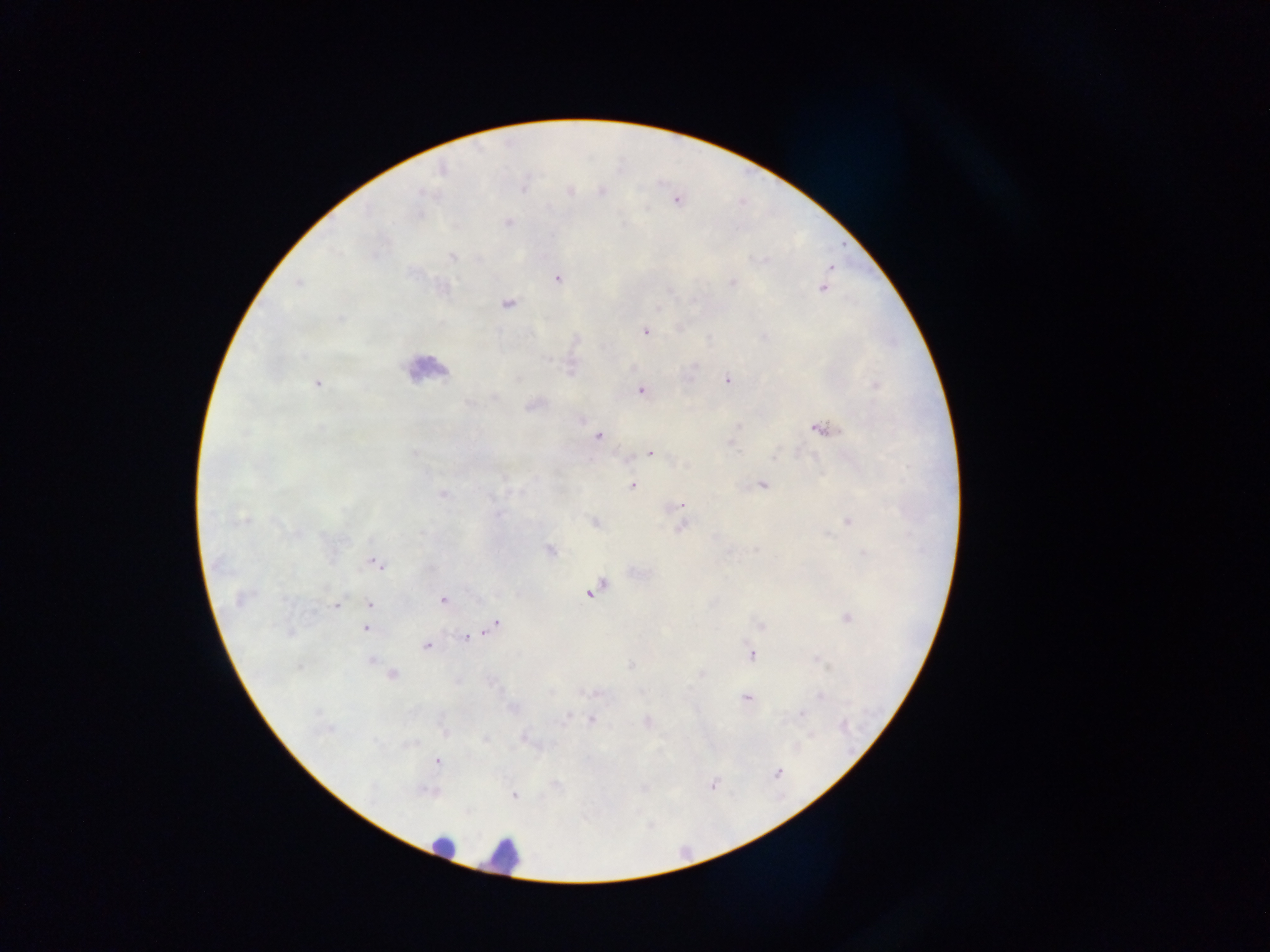
{
  "plasmodium_parasite_locations": "approximate centers as x y in pixels: 508 223; 452 256; 830 269; 557 278; 298 283; 733 284; 822 288; 507 304; 646 332; 695 366; 727 380; 318 383; 641 390; 824 429; 598 437; 650 453; 762 484; 633 485; 443 494; 680 505; 849 521; 681 527; 550 550; 376 564; 592 590; 238 600; 442 601; 369 604; 336 606; 847 618; 495 626; 761 626; 366 629; 466 637; 426 646; 751 654; 371 661; 393 674; 701 674; 746 698; 802 714; 437 761; 777 772; 712 785; 514 794",
  "country": "Ghana",
  "image_size": "1270×952 pixels",
  "capture": "mobile-phone photograph through a microscope",
  "leukocyte_locations": "approximate centers as x y in pixels: 424 368; 443 846; 501 855",
  "preparation": "thick blood smear",
  "field_of_view": "single"
}